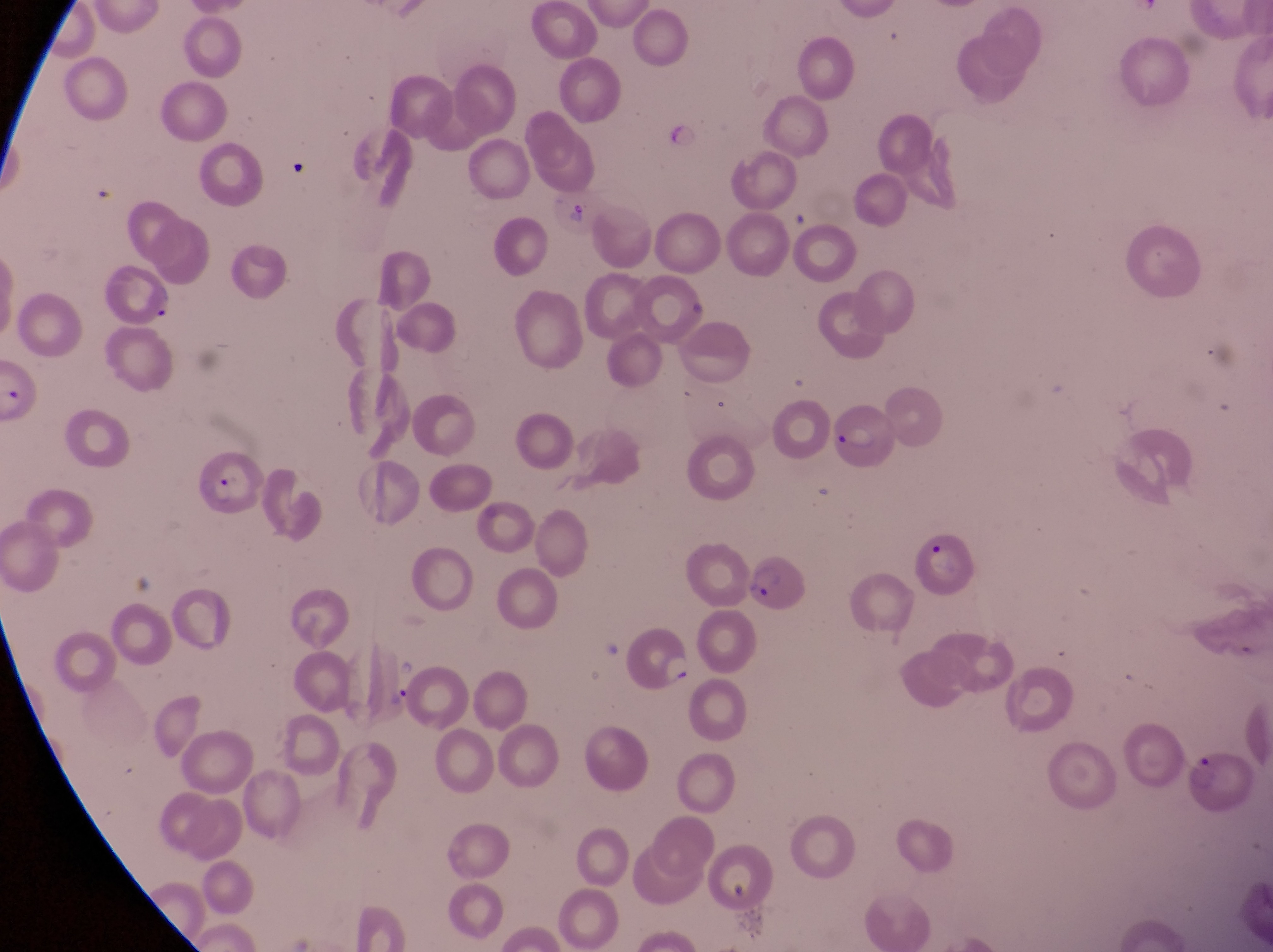

Approximate bounding boxes as {left, top, right, bottom} in pixels.
Summary:
  - Trophozoite locations: {664, 122, 711, 157}, {375, 674, 415, 714}
  - Parasitised red blood cell locations: {107, 262, 179, 330}, {829, 394, 891, 474}, {195, 452, 264, 517}, {911, 529, 980, 601}, {747, 556, 809, 619}, {619, 619, 697, 696}, {1186, 754, 1255, 812}
  - Artifact (platelet-like body, stain precipitate, or debris) locations: {278, 153, 310, 183}, {557, 200, 592, 228}
  - Magnification: 1000x
  - Image size: 1273×952 pixels
  - Field of view: single
  - Preparation: thin blood smear
  - Capture: smartphone photograph through the eyepiece of an Olympus CX-23 microscope
  - Country: Uganda